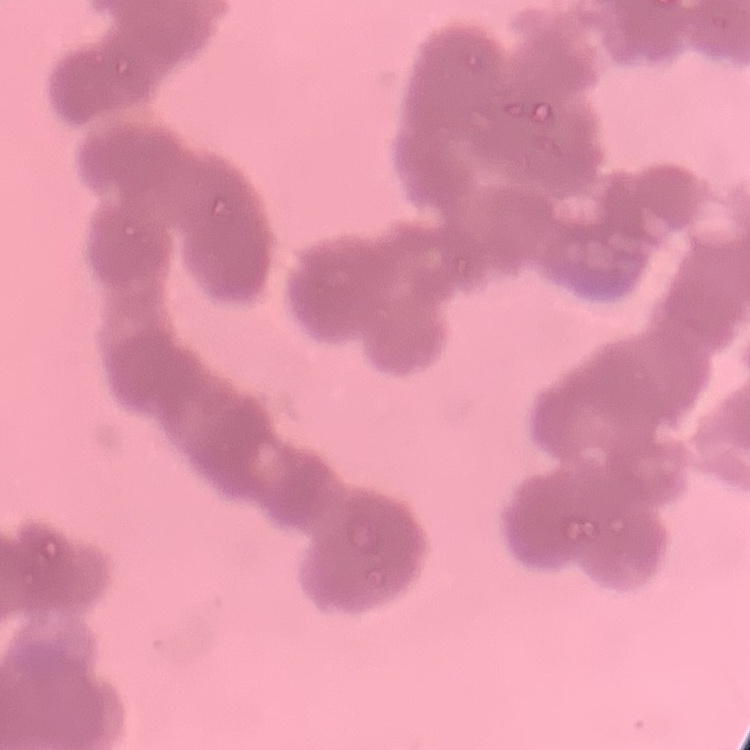

erythrocyte morphology = rouleaux formation
preparation = thin peripheral smear
image type = square crop of a larger photomicrograph
stain = Field's or Giemsa